Evaluate for parasitized red blood cells.
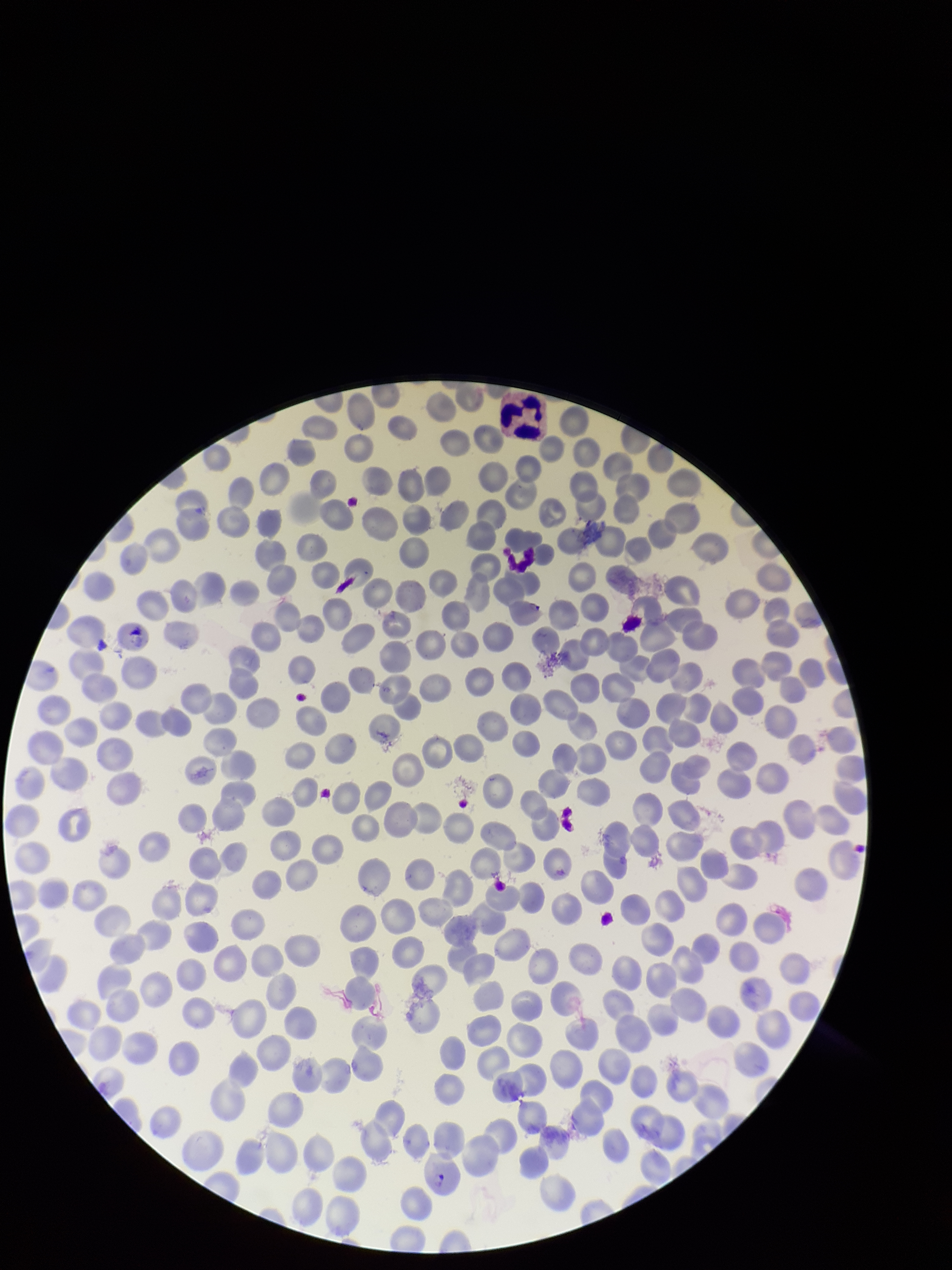

Detected.

Summary:
  - Species reported for this patient: Plasmodium falciparum
  - Field of view: single
  - Patient malaria status: positive
  - Capture: smartphone photograph through the microscope eyepiece
  - Image size: 952×1270 pixels
  - Red blood cell count: 285
  - Parasitized red blood cell count: 1
  - Stain: Giemsa
  - Preparation: thin smear